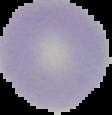

image size = 112×115 pixels
result = negative for Plasmodium parasites
image type = cell region segmented out of the field of view; surrounding area masked to black
preparation = thin blood film